Give the position of every malaria parasite.
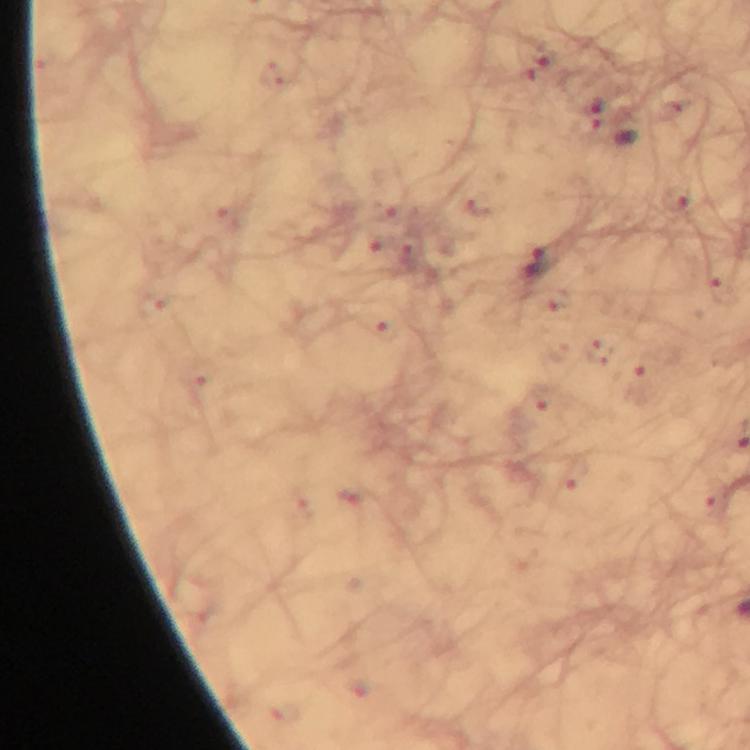
Approximate centers as (x, y) in pixels.
Malaria parasites: (536, 263).

Summary:
  - Preparation: thick blood smear
  - Capture: smartphone camera through the microscope
  - Immersion oil: applied
  - Context: from a malaria diagnostic workup
  - Magnification: 100x
  - Stain: Giemsa
  - Cropped from: one field of view
  - Image size: 750×750 pixels